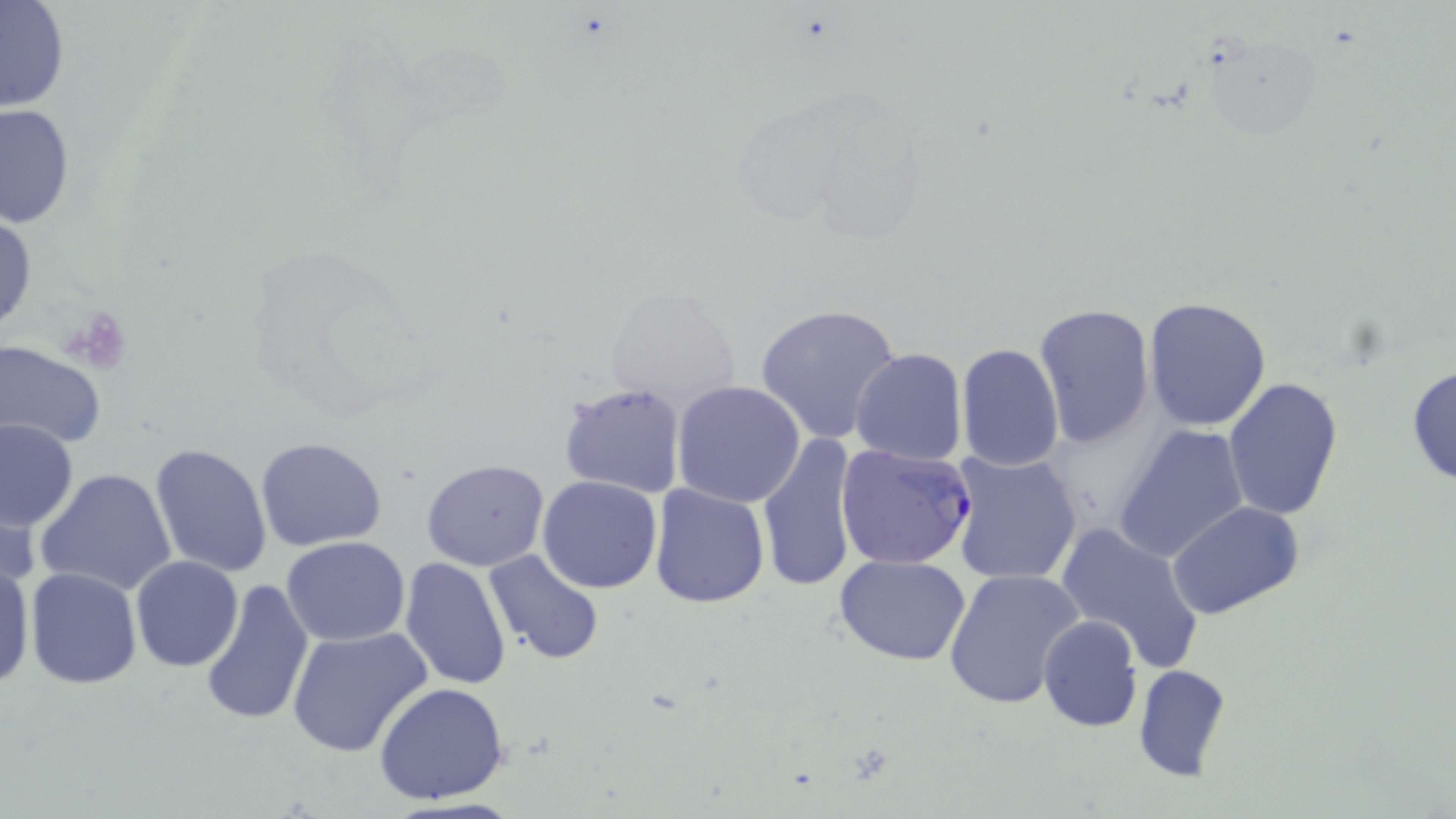

slide-level diagnosis = Plasmodium falciparum
platelet locations = approximate bounding boxes as named x1/y1/x2/y2 corners in pixels: (x1=67, y1=308, x2=131, y2=372)
modality = optical microscopy
field of view = one of a larger specimen
image size = 1456×819 pixels
uninfected red blood cell locations = approximate bounding boxes as named x1/y1/x2/y2 corners in pixels: (x1=0, y1=2, x2=70, y2=113), (x1=1206, y1=32, x2=1318, y2=143), (x1=1, y1=104, x2=75, y2=230), (x1=1, y1=211, x2=37, y2=335), (x1=599, y1=285, x2=739, y2=412), (x1=1142, y1=298, x2=1272, y2=431), (x1=1034, y1=303, x2=1156, y2=448), (x1=752, y1=304, x2=903, y2=447), (x1=0, y1=340, x2=105, y2=452), (x1=956, y1=342, x2=1064, y2=470), (x1=850, y1=348, x2=967, y2=465), (x1=1406, y1=363, x2=1456, y2=487), (x1=1223, y1=378, x2=1344, y2=522), (x1=557, y1=381, x2=686, y2=500), (x1=673, y1=381, x2=806, y2=507), (x1=1, y1=417, x2=78, y2=531), (x1=1112, y1=426, x2=1249, y2=564), (x1=758, y1=432, x2=860, y2=593), (x1=254, y1=436, x2=388, y2=550), (x1=150, y1=442, x2=272, y2=578), (x1=949, y1=451, x2=1083, y2=585), (x1=421, y1=458, x2=549, y2=570), (x1=36, y1=466, x2=178, y2=597), (x1=538, y1=474, x2=663, y2=594), (x1=648, y1=483, x2=771, y2=608), (x1=1, y1=485, x2=39, y2=597), (x1=1167, y1=501, x2=1306, y2=621), (x1=1054, y1=523, x2=1205, y2=671), (x1=280, y1=537, x2=411, y2=646), (x1=483, y1=550, x2=605, y2=666), (x1=0, y1=552, x2=34, y2=691), (x1=833, y1=553, x2=972, y2=665), (x1=130, y1=557, x2=242, y2=672), (x1=399, y1=557, x2=512, y2=690), (x1=943, y1=566, x2=1085, y2=710), (x1=24, y1=567, x2=143, y2=689), (x1=199, y1=578, x2=315, y2=729), (x1=1037, y1=614, x2=1142, y2=732), (x1=287, y1=627, x2=432, y2=759), (x1=1132, y1=664, x2=1233, y2=783), (x1=373, y1=681, x2=512, y2=806)
stain = May-Grünwald-Giemsa
Plasmodium falciparum-infected red blood cell locations = approximate bounding boxes as named x1/y1/x2/y2 corners in pixels: (x1=835, y1=443, x2=975, y2=571)
magnification = 1000x
preparation = thin blood film